Locate and identify every blood parasite.
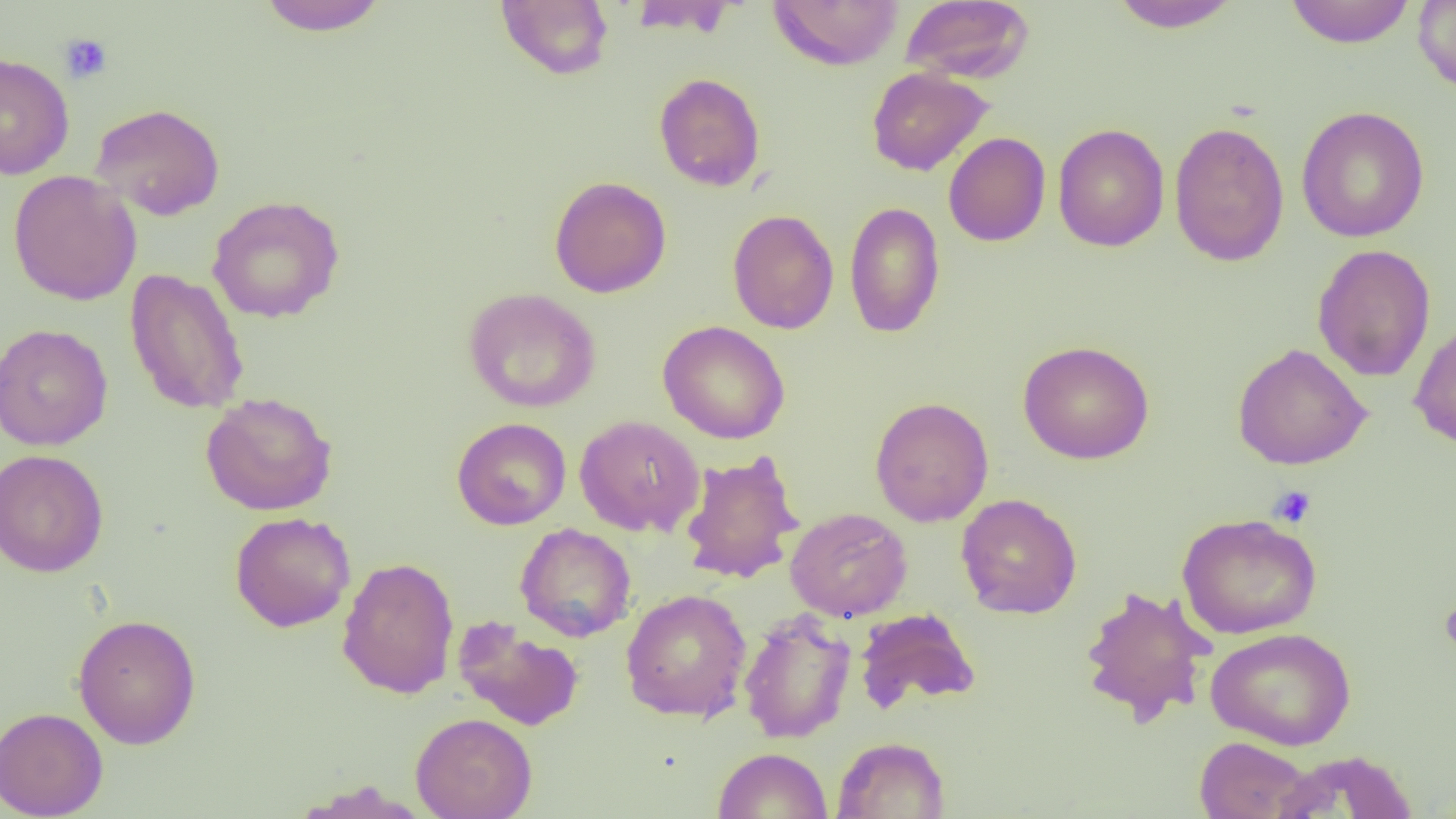

No blood parasites observed.

slide-level diagnosis = negative for blood parasites
uninfected red blood cell locations = approximate bounding boxes as (x1,y1)-(x2,y2) corner pairs in pixels: (256,0)-(389,36), (495,0)-(614,80), (626,0)-(739,37), (767,0)-(904,70), (899,0)-(1035,84), (1107,0)-(1243,32), (1412,0)-(1456,95), (1284,1)-(1416,48), (0,52)-(74,180), (867,67)-(994,176), (653,72)-(766,192), (90,103)-(226,221), (1296,106)-(1430,243), (1169,120)-(1289,267), (1053,123)-(1170,252), (943,132)-(1051,246), (8,170)-(142,306), (549,176)-(672,298), (207,195)-(345,323), (844,201)-(945,338), (727,209)-(839,334), (1312,243)-(1436,382), (124,268)-(249,415), (463,287)-(601,413), (1408,317)-(1456,451), (658,321)-(791,444), (0,323)-(113,451), (1017,340)-(1155,464), (1232,343)-(1371,470), (200,392)-(338,516), (869,396)-(994,527), (574,415)-(704,537), (452,417)-(571,530), (0,449)-(108,578), (678,450)-(803,585), (956,493)-(1082,619), (785,507)-(912,622), (230,512)-(356,632), (1176,513)-(1322,639), (515,523)-(636,642), (337,556)-(459,698), (1078,584)-(1215,726), (621,589)-(752,722), (854,608)-(980,714), (739,609)-(856,744), (72,613)-(201,749), (452,616)-(584,731), (1205,627)-(1357,750), (0,706)-(108,819), (411,712)-(537,819), (832,736)-(950,818), (1194,736)-(1314,818), (713,747)-(832,819), (1270,750)-(1419,817)
field of view = single
modality = light microscopy
magnification = 1000x
image size = 1456×819 pixels
platelet locations = approximate bounding boxes as (x1,y1)-(x2,y2) corner pairs in pixels: (59,33)-(113,85), (1268,485)-(1317,529), (1439,596)-(1456,658)
preparation = thin blood smear